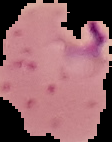

Cell region segmented out of the field of view; the surrounding area is masked to black. Malaria status: parasitized. Image is 112×142 pixels. From a thin blood smear.